Assess the morphology of the red blood cells.
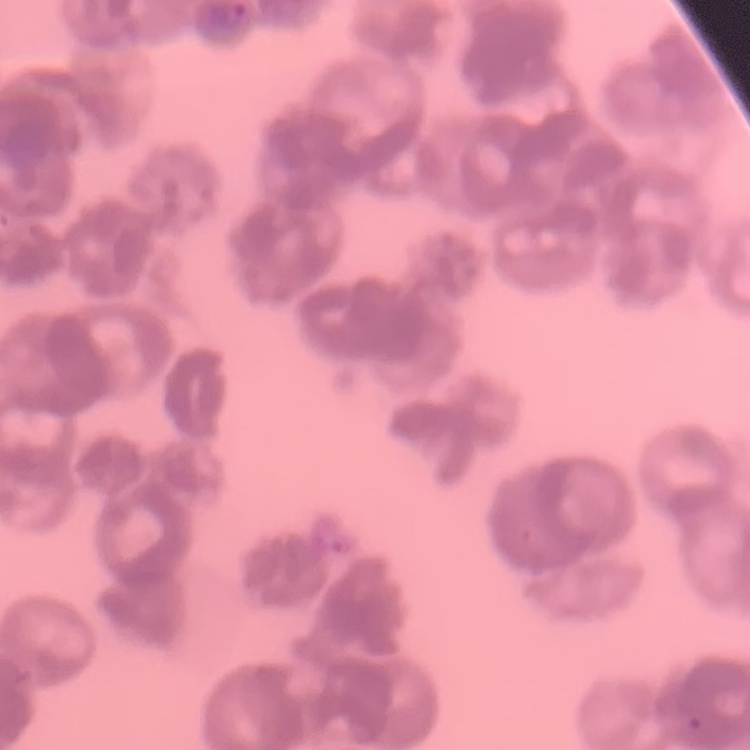

They show rouleaux formation.

Square crop of a larger photomicrograph. Thin blood film. Field's or Giemsa stain.